Classify this cell by malaria status.
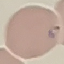
It is parasitized.

Acquired by smartphone through the microscope eyepiece. Thin blood film. Giemsa stain. Cell patch, automatically extracted from a larger field of view and resized to 64 × 64 pixels.